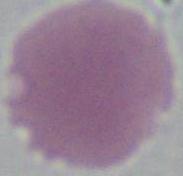
Summary:
  - Modality: photomicrograph
  - Identification: erythrocyte
  - Magnification: 1000x